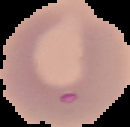

{
  "image_type": "cell region segmented out of the field of view; surrounding area masked to black",
  "result": "no Plasmodium parasites detected",
  "preparation": "thin blood smear",
  "image_size": "130×127 pixels"
}